Locate and identify every blood parasite.
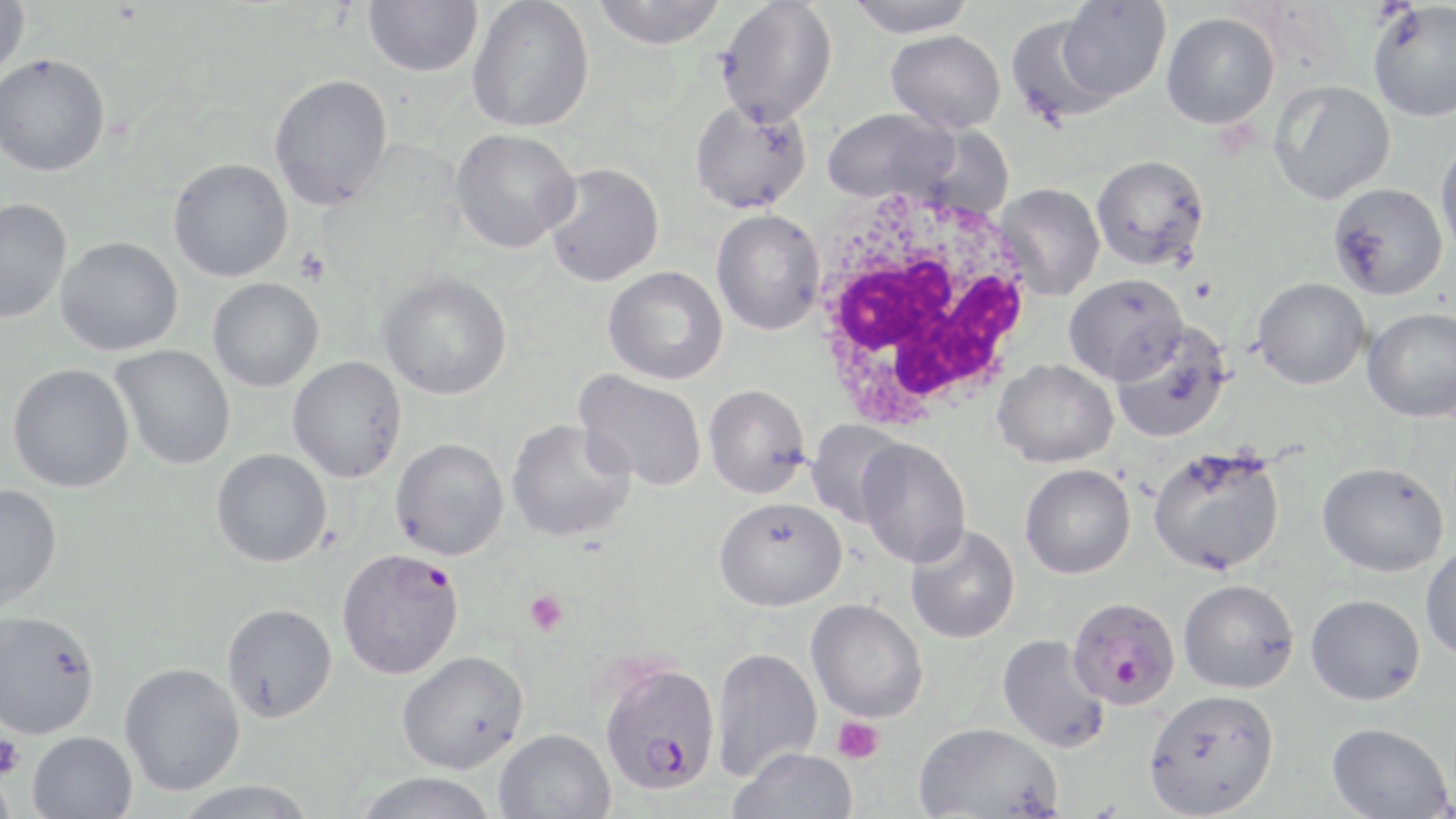
Approximate bounding boxes as (x1, y1, x2, y2) in pixels.
Plasmodium falciparum-infected red blood cells: (336, 548, 464, 679), (1067, 595, 1181, 708), (600, 662, 722, 795).
No Plasmodium ovale, Plasmodium malariae, Plasmodium vivax, Babesia divergens, or Trypanosoma brucei observed.

{
  "slide_level_diagnosis": "Plasmodium falciparum",
  "uninfected_red_blood_cell_locations": "approximate bounding boxes as (x1, y1, x2, y2) in pixels: (0, 0, 29, 81), (363, 0, 483, 77), (591, 0, 728, 49), (844, 0, 977, 38), (466, 1, 594, 133), (715, 1, 839, 126), (1057, 1, 1170, 101), (1367, 3, 1456, 122), (1161, 12, 1279, 129), (1004, 14, 1116, 127), (886, 29, 1006, 133), (0, 53, 111, 177), (268, 73, 392, 211), (1270, 80, 1395, 204), (690, 97, 812, 214), (821, 107, 963, 205), (450, 129, 581, 253), (1435, 134, 1456, 261), (1091, 154, 1211, 271), (168, 158, 293, 282), (543, 163, 664, 287), (995, 182, 1105, 300), (1328, 182, 1449, 300), (0, 198, 71, 324), (711, 210, 825, 335), (55, 237, 183, 357), (603, 266, 728, 385), (379, 271, 512, 400), (1063, 273, 1187, 384), (1252, 277, 1370, 389), (208, 278, 324, 392), (1362, 307, 1456, 422), (1109, 319, 1232, 443), (111, 344, 236, 470), (287, 356, 407, 483), (992, 358, 1119, 468), (7, 363, 134, 492), (574, 370, 708, 492), (703, 384, 812, 498), (505, 419, 636, 542), (805, 419, 909, 527), (390, 437, 509, 560), (856, 438, 972, 568), (1147, 445, 1286, 577), (211, 448, 332, 567), (1317, 461, 1450, 577), (1020, 464, 1136, 579), (0, 484, 62, 612), (714, 497, 847, 611), (905, 522, 1020, 644), (1420, 541, 1456, 662), (1178, 579, 1299, 694), (1305, 594, 1425, 705), (806, 599, 928, 723), (221, 603, 337, 723), (0, 610, 100, 740), (997, 634, 1111, 754), (710, 646, 823, 781), (396, 650, 529, 773), (119, 662, 245, 795), (1144, 688, 1280, 818), (913, 721, 1063, 818), (1327, 721, 1452, 818), (494, 728, 616, 819), (27, 731, 138, 818), (728, 748, 859, 819), (0, 768, 17, 819), (352, 771, 498, 818), (175, 779, 319, 818)",
  "magnification": "1000x",
  "platelet_locations": "approximate bounding boxes as (x1, y1, x2, y2) in pixels: (295, 248, 331, 286), (525, 589, 569, 636), (832, 716, 886, 764), (0, 733, 25, 779)",
  "image_size": "1456×819 pixels",
  "modality": "optical microscopy",
  "stain": "May-Grünwald-Giemsa",
  "white_blood_cell_locations": "approximate bounding boxes as (x1, y1, x2, y2) in pixels: (806, 185, 1042, 428)",
  "field_of_view": "single",
  "preparation": "thin blood film"
}